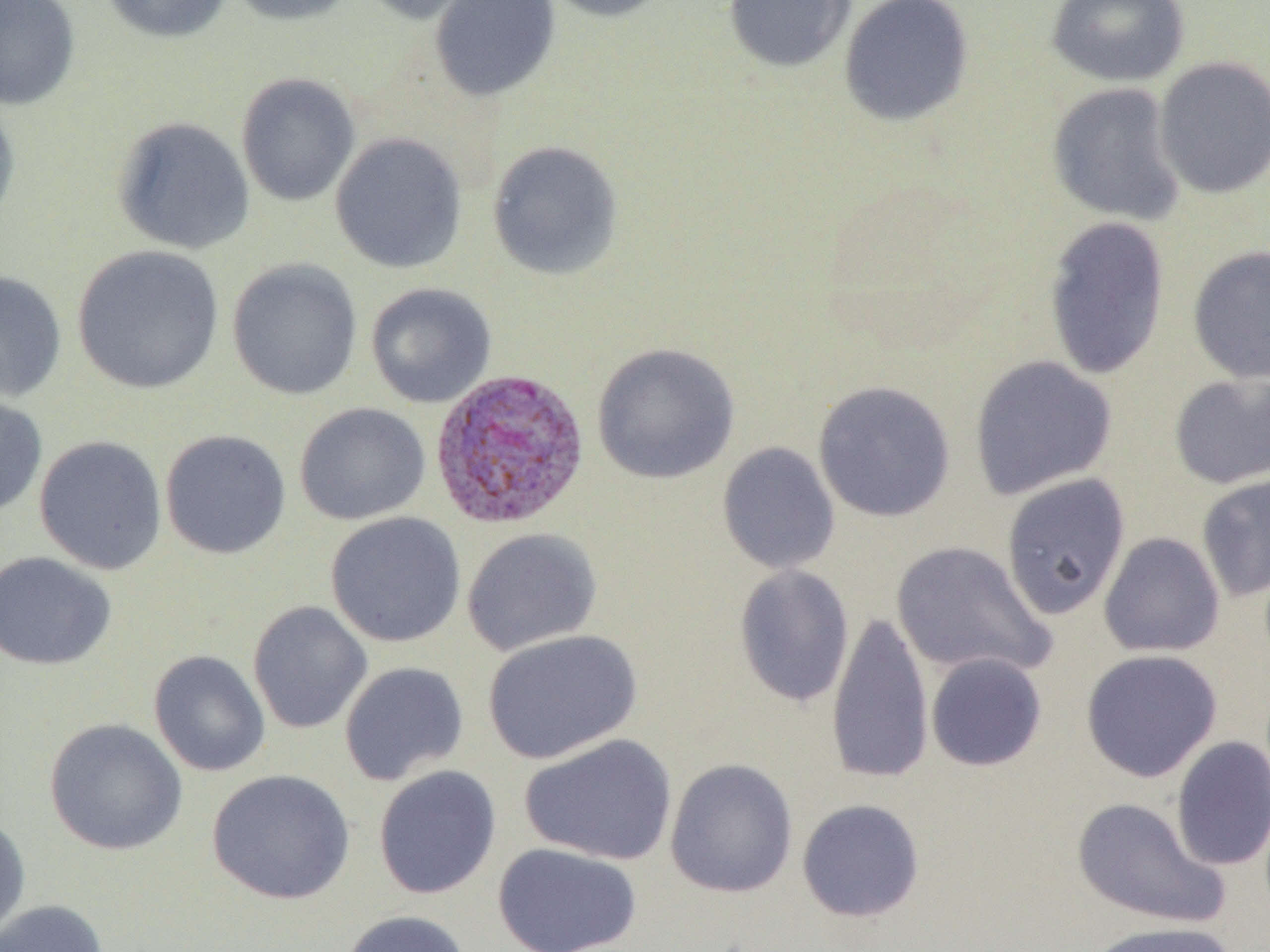
Summary:
  - Coordinate format: approximate bounding boxes as (x1, y1, x2, y2) in pixels
  - Plasmodium vivax-infected red blood cell locations: (429, 367, 590, 531)
  - Uninfected red blood cell locations: (1, 0, 81, 110), (99, 0, 233, 44), (225, 0, 359, 26), (356, 0, 492, 25), (429, 0, 561, 103), (537, 0, 677, 23), (723, 0, 857, 73), (838, 0, 975, 127), (1045, 0, 1190, 87), (1154, 56, 1270, 199), (235, 72, 361, 207), (1046, 82, 1187, 226), (0, 96, 21, 231), (112, 116, 255, 255), (329, 132, 468, 273), (487, 140, 625, 281), (1042, 215, 1171, 381), (71, 245, 225, 394), (1187, 245, 1270, 384), (227, 258, 363, 401), (0, 270, 68, 403), (365, 282, 497, 408), (591, 342, 740, 484), (968, 355, 1118, 500), (1168, 373, 1270, 490), (812, 380, 956, 522), (0, 393, 48, 520), (294, 402, 431, 525), (159, 429, 292, 560), (33, 435, 168, 575), (717, 442, 840, 575), (1196, 471, 1270, 602), (1000, 472, 1131, 620), (324, 511, 466, 648), (461, 527, 602, 656), (1099, 532, 1225, 658), (890, 540, 1057, 680), (0, 551, 117, 671), (733, 564, 855, 708), (247, 600, 372, 734), (826, 608, 934, 786), (481, 629, 642, 764), (1080, 648, 1223, 783), (148, 650, 271, 777), (926, 653, 1047, 771), (339, 661, 469, 786), (44, 718, 188, 856), (519, 733, 678, 866), (1170, 736, 1270, 872), (664, 758, 798, 898), (372, 765, 502, 900), (206, 769, 356, 905), (1070, 796, 1229, 929), (796, 798, 925, 923), (0, 813, 31, 944), (492, 842, 643, 952), (0, 899, 109, 952), (338, 909, 473, 952), (1086, 920, 1239, 952)
  - Slide-level diagnosis: Plasmodium vivax
  - Image size: 1270×952 pixels
  - Preparation: thin blood film
  - Modality: light microscopy
  - Magnification: 1000x
  - Field of view: single